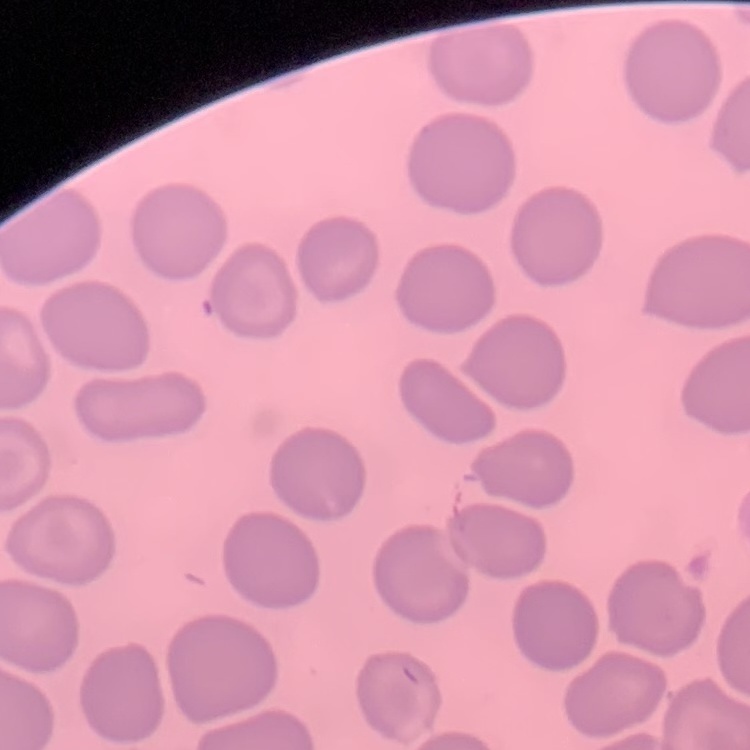
Summary:
  - Erythrocyte morphology: no rouleaux formation
  - Preparation: thin peripheral smear
  - Stain: Field's or Giemsa
  - Image type: square crop of a larger photomicrograph